Point out every malaria parasite and every leukocyte.
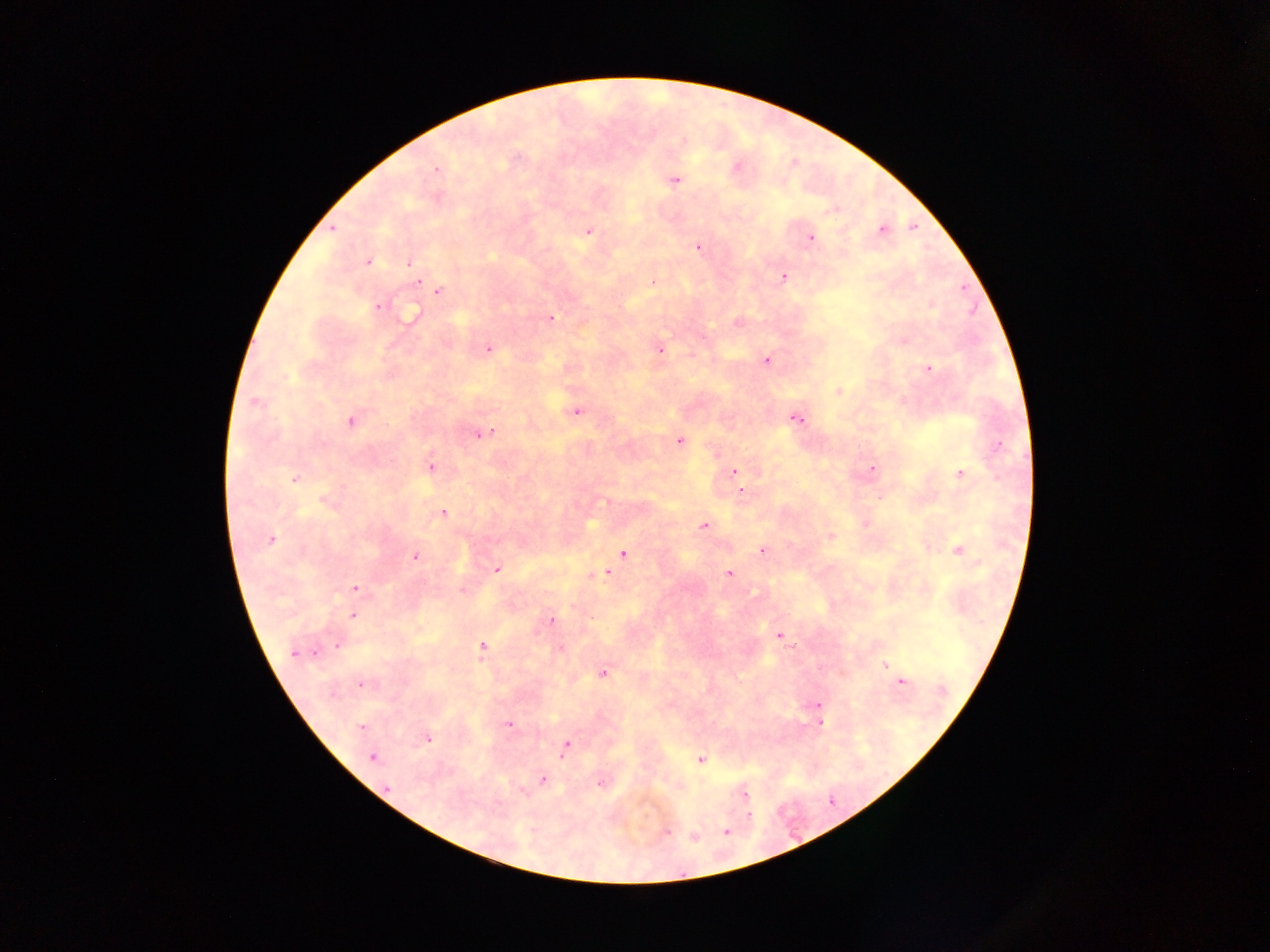

Approximate centers as {x, y} in pixels.
Malaria parasites: {435, 169}, {675, 180}, {881, 230}, {588, 231}, {812, 237}, {697, 247}, {368, 262}, {407, 264}, {782, 276}, {654, 279}, {416, 281}, {438, 291}, {377, 307}, {551, 318}, {486, 348}, {660, 348}, {766, 360}, {929, 369}, {576, 411}, {795, 418}, {352, 421}, {492, 429}, {480, 436}, {679, 440}, {432, 465}, {872, 468}, {733, 470}, {958, 473}, {295, 479}, {741, 490}, {444, 512}, {704, 526}, {272, 538}, {958, 549}, {764, 550}, {623, 553}, {415, 556}, {497, 568}, {606, 571}, {729, 574}, {355, 587}, {352, 614}, {551, 619}, {780, 635}, {338, 646}, {482, 646}, {561, 648}, {292, 652}, {884, 665}, {604, 673}, {899, 680}, {359, 686}, {818, 703}, {509, 725}, {821, 725}, {361, 728}, {428, 739}, {567, 744}, {372, 756}, {702, 759}, {543, 780}, {746, 795}, {831, 802}, {748, 816}, {728, 831}, {669, 832}.
No leukocytes observed.

country = Ghana
preparation = thick blood film
field of view = single
capture = mobile-phone photograph through a microscope
image size = 1270×952 pixels